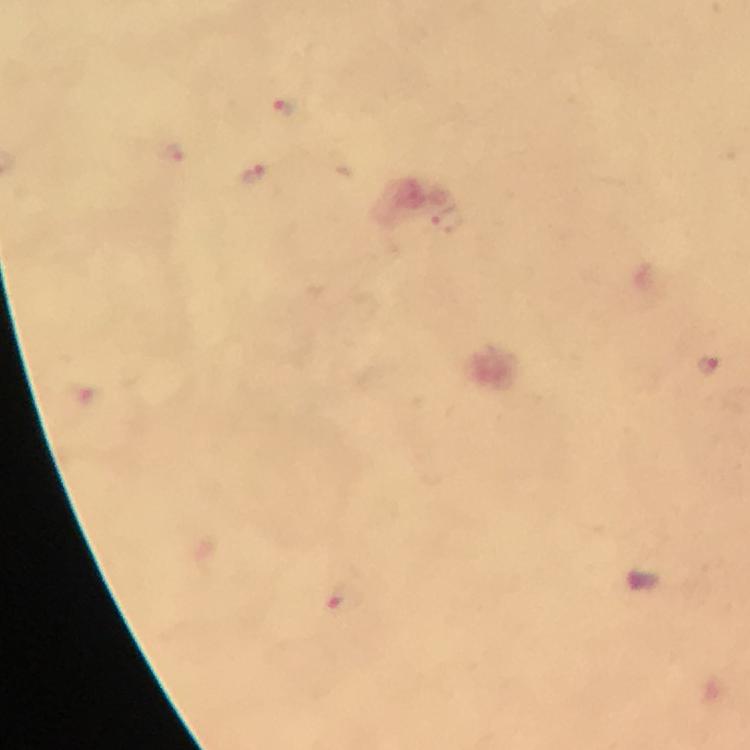

Approximate centers as [x, y] in pixels.
Summary:
  - Malaria parasite locations: [283, 107], [174, 155], [250, 177], [707, 364], [342, 601]
  - Context: from a diagnostic examination for malaria
  - Immersion oil: used
  - Capture: smartphone mounted on the microscope
  - Image size: 750×750 pixels
  - Cropped from: one field of view
  - Stain: Giemsa
  - Magnification: 100x
  - Preparation: thick blood film